Assess this cell for malaria.
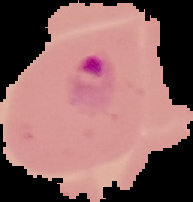

Parasitized.

Summary:
  - Image size: 193×202 pixels
  - Preparation: thin blood smear
  - Image type: cell region segmented out of the field of view; surrounding area masked to black